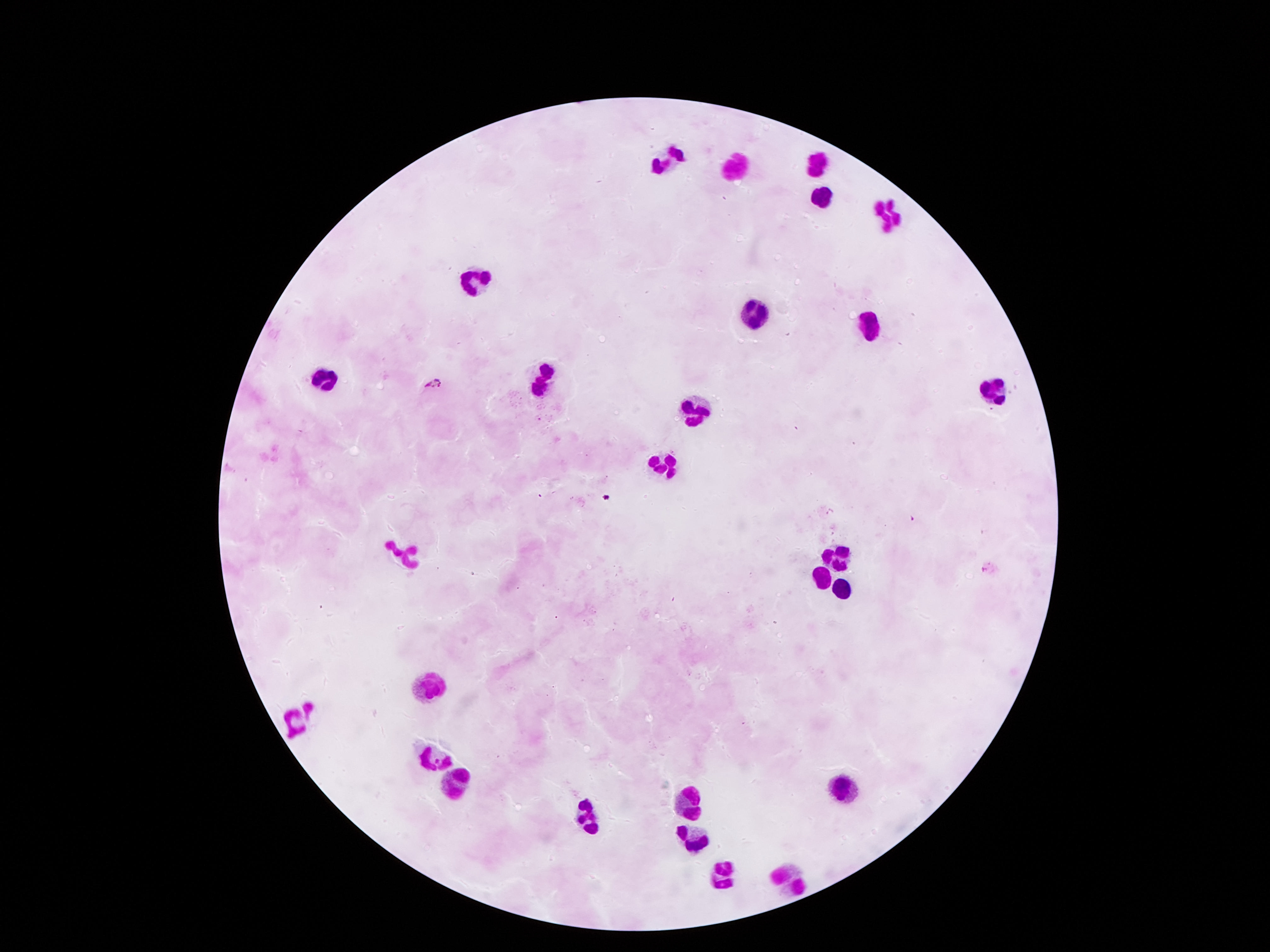 Approximate centers as (x, y) in pixels. Leukocyte locations: (670, 161), (820, 164), (738, 171), (822, 196), (892, 212), (476, 281), (751, 312), (866, 321), (321, 377), (545, 377), (995, 390), (697, 407), (662, 457), (836, 548), (406, 554), (823, 570), (843, 587), (430, 685), (293, 725), (431, 756), (457, 785), (842, 787), (688, 796), (590, 814), (689, 831), (714, 876), (789, 876). Giemsa-stained preparation. Image is 1270×952 pixels. Thick peripheral-blood smear. One field from this slide. 100x magnification. Photographed through the microscope eyepiece with a smartphone camera. Patient malaria status: negative.